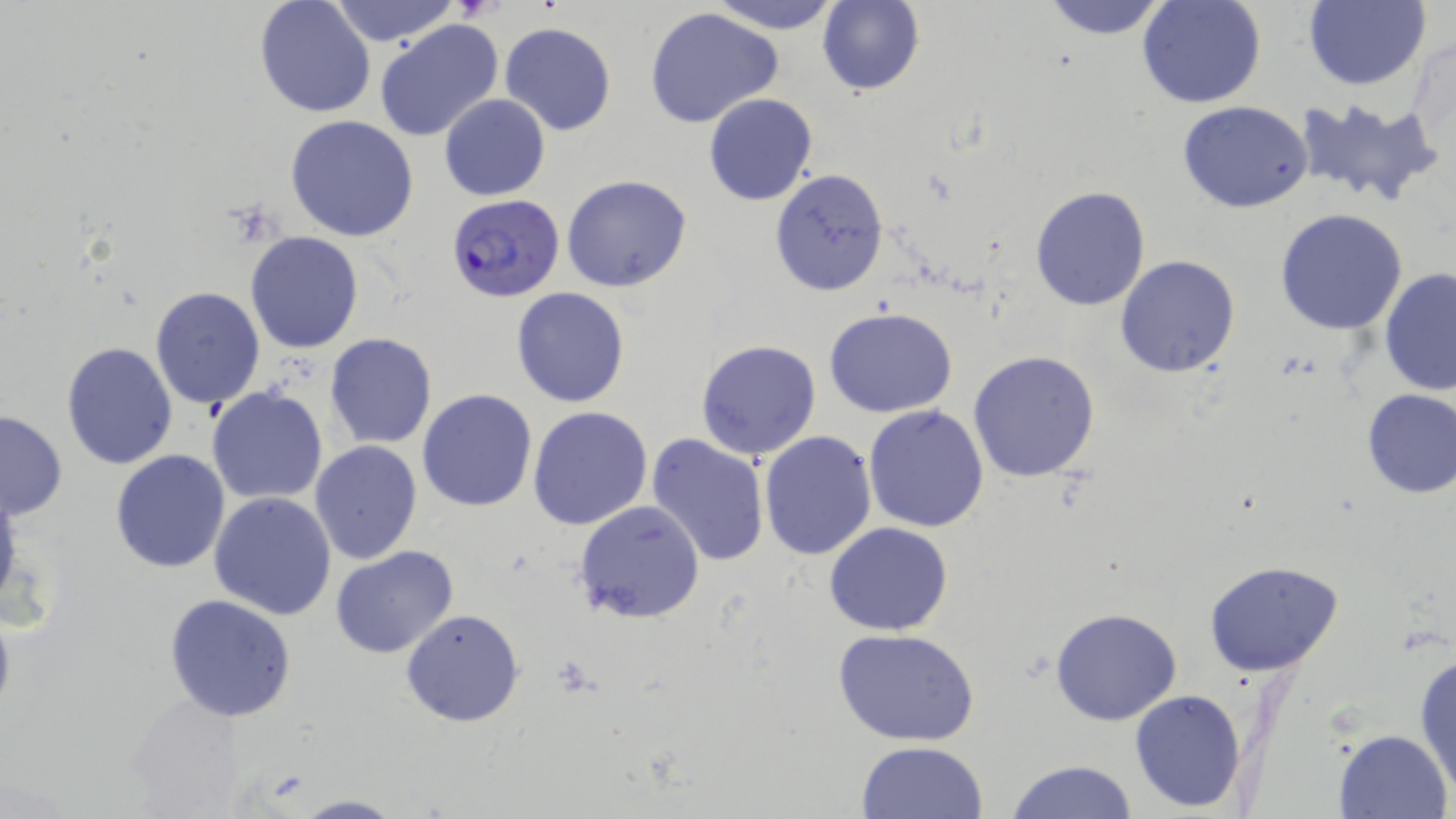

Summary:
  - Coordinate format: approximate bounding boxes as named x1/y1/x2/y2 corners in pixels
  - Plasmodium falciparum-infected red blood cell locations: (x1=446, y1=196, x2=563, y2=303)
  - Uninfected red blood cell locations: (x1=326, y1=0, x2=460, y2=46), (x1=706, y1=0, x2=842, y2=35), (x1=1039, y1=0, x2=1173, y2=40), (x1=1137, y1=0, x2=1268, y2=110), (x1=1301, y1=0, x2=1432, y2=90), (x1=254, y1=1, x2=376, y2=118), (x1=816, y1=1, x2=924, y2=96), (x1=644, y1=6, x2=785, y2=128), (x1=373, y1=19, x2=503, y2=143), (x1=499, y1=22, x2=617, y2=135), (x1=1407, y1=37, x2=1456, y2=158), (x1=702, y1=93, x2=817, y2=206), (x1=439, y1=94, x2=551, y2=201), (x1=1291, y1=98, x2=1442, y2=207), (x1=1177, y1=101, x2=1316, y2=214), (x1=285, y1=115, x2=419, y2=242), (x1=770, y1=168, x2=888, y2=295), (x1=561, y1=174, x2=693, y2=293), (x1=1029, y1=186, x2=1150, y2=311), (x1=1274, y1=208, x2=1409, y2=335), (x1=246, y1=232, x2=363, y2=353), (x1=1115, y1=255, x2=1241, y2=377), (x1=1379, y1=268, x2=1456, y2=395), (x1=150, y1=286, x2=265, y2=410), (x1=511, y1=287, x2=630, y2=408), (x1=825, y1=308, x2=957, y2=419), (x1=325, y1=332, x2=438, y2=451), (x1=695, y1=339, x2=822, y2=462), (x1=61, y1=341, x2=177, y2=468), (x1=968, y1=349, x2=1102, y2=483), (x1=206, y1=386, x2=328, y2=505), (x1=417, y1=389, x2=537, y2=513), (x1=1358, y1=389, x2=1456, y2=499), (x1=863, y1=405, x2=990, y2=534), (x1=528, y1=407, x2=653, y2=530), (x1=0, y1=410, x2=68, y2=520), (x1=758, y1=430, x2=879, y2=559), (x1=647, y1=433, x2=771, y2=567), (x1=309, y1=440, x2=423, y2=564), (x1=110, y1=448, x2=231, y2=573), (x1=0, y1=481, x2=24, y2=616), (x1=209, y1=491, x2=337, y2=620), (x1=572, y1=500, x2=705, y2=624), (x1=825, y1=522, x2=952, y2=636), (x1=330, y1=546, x2=460, y2=660), (x1=1204, y1=561, x2=1346, y2=678), (x1=164, y1=593, x2=297, y2=722), (x1=0, y1=604, x2=16, y2=726), (x1=1049, y1=608, x2=1181, y2=726), (x1=402, y1=609, x2=524, y2=727), (x1=835, y1=628, x2=981, y2=746), (x1=1414, y1=651, x2=1456, y2=796), (x1=1128, y1=689, x2=1248, y2=812), (x1=122, y1=694, x2=255, y2=815), (x1=1334, y1=728, x2=1453, y2=818), (x1=856, y1=741, x2=987, y2=819), (x1=1007, y1=759, x2=1136, y2=819), (x1=291, y1=793, x2=403, y2=818)
  - Slide-level diagnosis: Plasmodium falciparum
  - Stain: May-Grünwald-Giemsa
  - Magnification: 1000x
  - Field of view: one of a larger specimen
  - Image size: 1456×819 pixels
  - Preparation: thin blood smear
  - Modality: optical microscopy